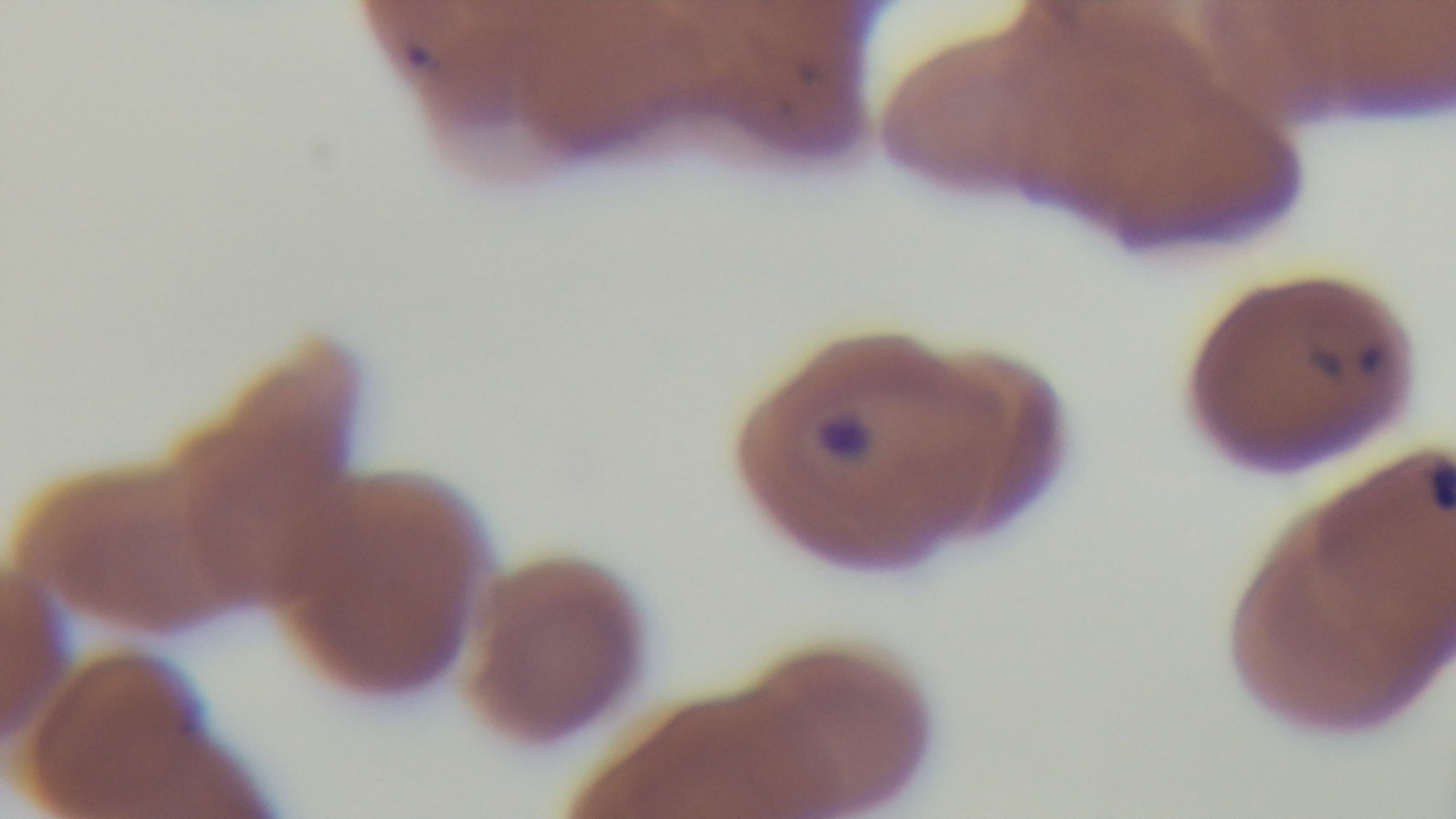
field_of_view: one from the slide
preparation: thin
stain: Giemsa
malaria_status: positive
modality: light microscopy
objective: 100x oil immersion
capture: mounted 4K digital camera